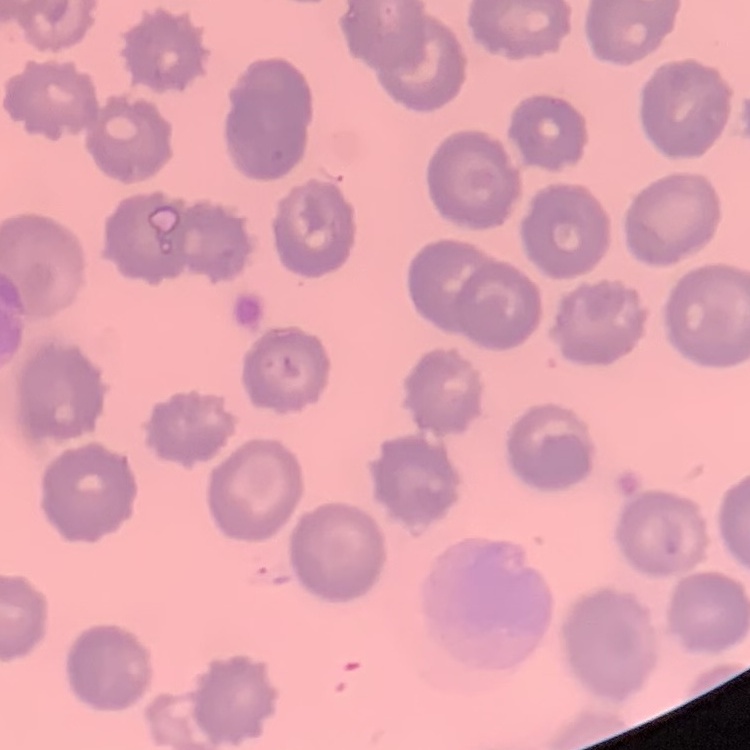 The erythrocytes show no rouleaux formation. Square crop of a larger photomicrograph. Thin peripheral smear. Stained with either Field's or Giemsa.